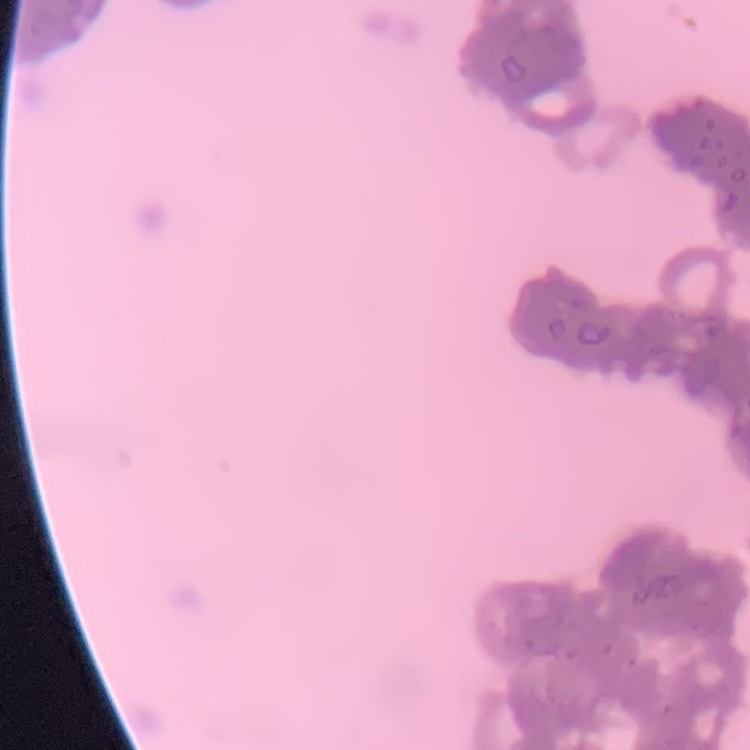

The erythrocytes show rouleaux formation. Stained with either Field's or Giemsa. Thin blood smear. Square crop of a larger photomicrograph.